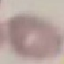 Malaria status: uninfected. Thin blood smear. Automatically extracted cell patch, resized to 64 × 64 pixels. Giemsa stain. Photographed with a smartphone camera at the microscope eyepiece.